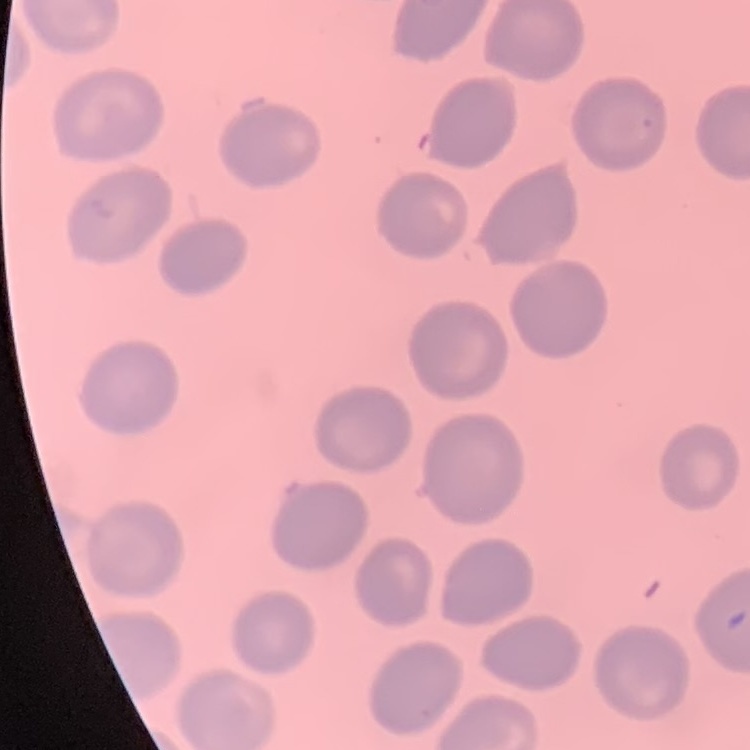

red blood cell morphology = no rouleaux formation
preparation = thin peripheral smear
image type = one tile cut from a larger photomicrograph
stain = Field's or Giemsa